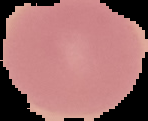

image type = cell region segmented out of the field of view; surrounding area masked to black
image size = 148×121 pixels
preparation = thin blood film
result = no Plasmodium parasites seen